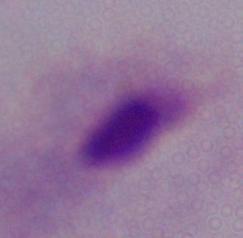

identification: trichomonad
modality: photomicrograph
magnification: 1000x